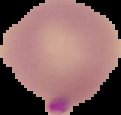

Image is 121×115 pixels. Malaria status: parasitized. The area outside the segmented cell region is set to black. From a thin blood film.